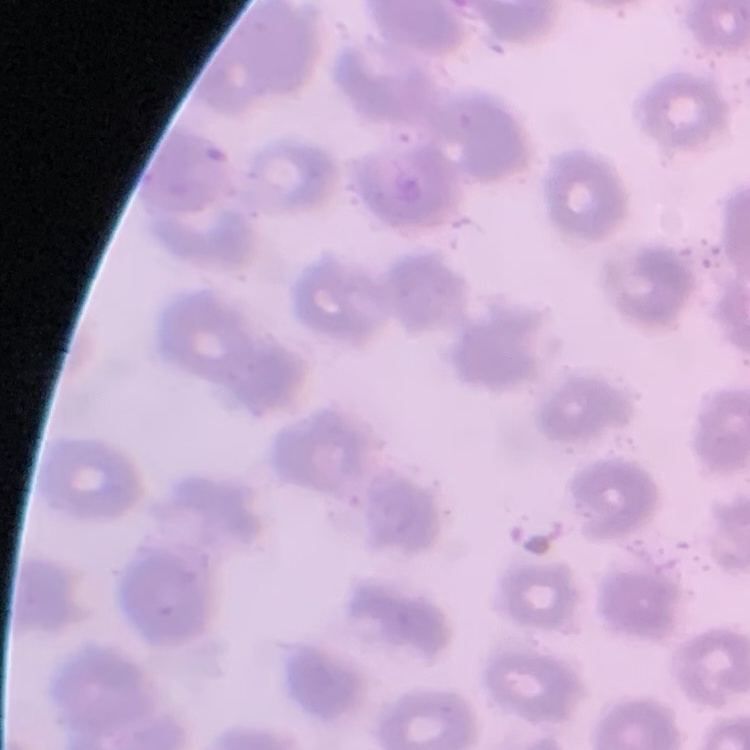
The red blood cells show no rouleaux formation. Thin blood smear. One tile cut from a larger photomicrograph. Field's or Giemsa stain.